Name the parasite shown.
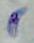

Toxoplasma gondii.

modality = micrograph
magnification = 1000x